Comment on the morphology of the red blood cells.
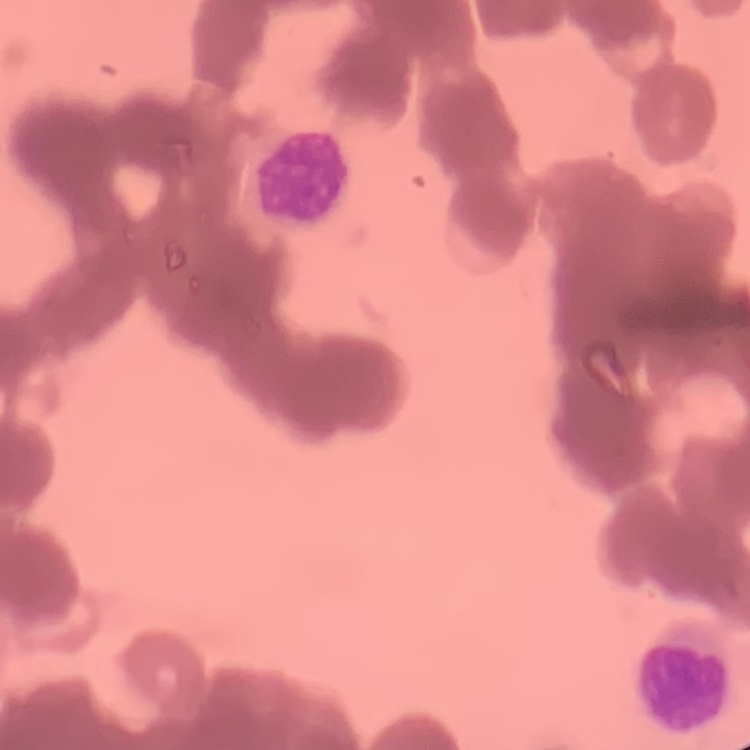
They show rouleaux formation.

Square crop of a larger photomicrograph. Thin blood film. Field's or Giemsa stain.